Assess this cell for malaria.
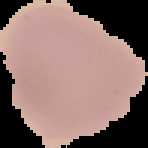

It is uninfected.

Cell region segmented out of the field of view; the surrounding area is masked to black. From a thin blood smear. Image is 148×148 pixels.